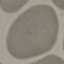

malaria status = uninfected
preparation = thin smear
stain = Giemsa
capture = smartphone camera at the microscope eyepiece
image type = automatically extracted cell patch, resized to 64 × 64 pixels